Give the extent of all uninfected red blood cells.
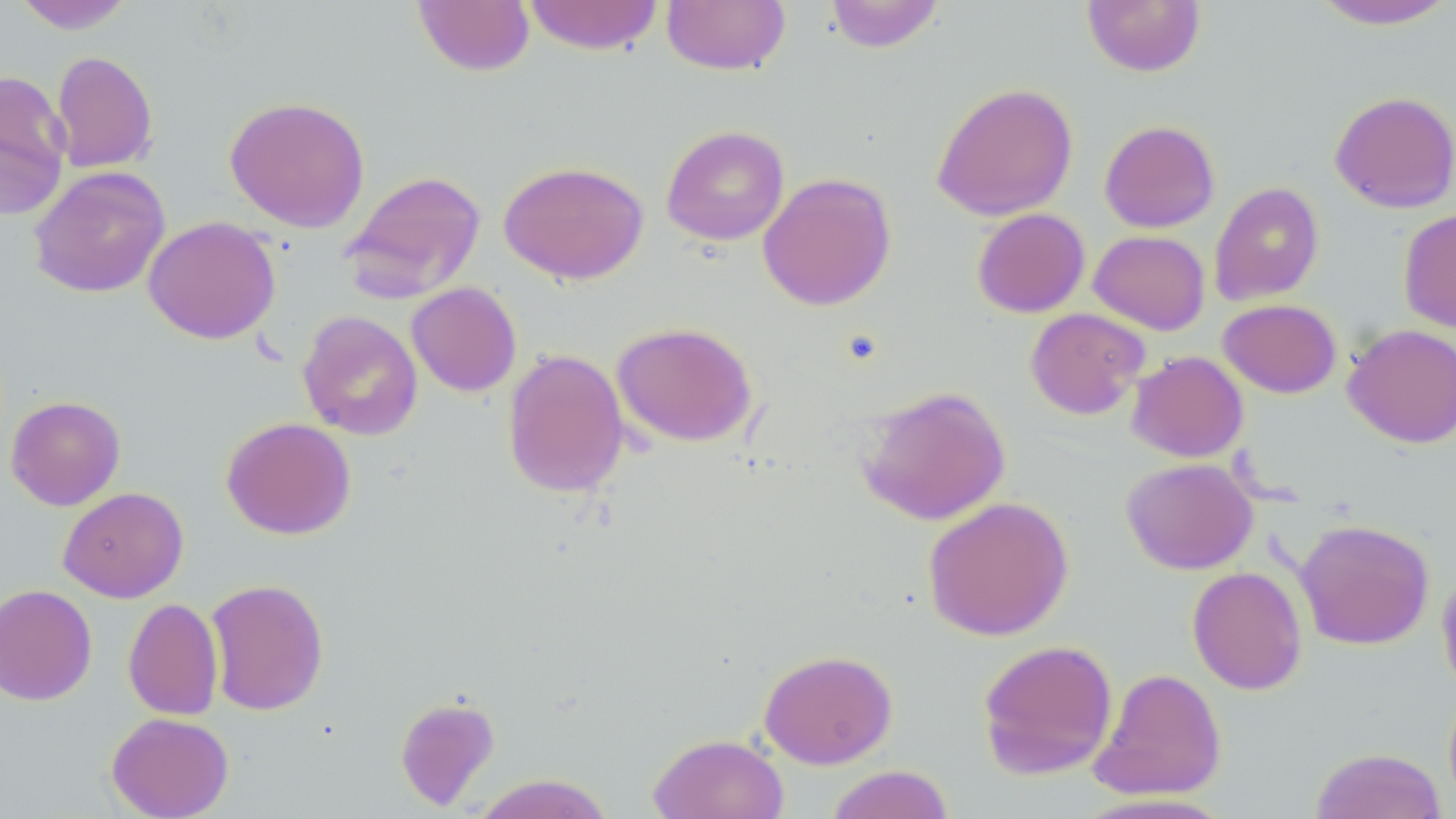
Approximate bounding boxes as (x1,y1)-(x2,y2) corner pairs in pixels.
Uninfected red blood cells: (521,0)-(665,55), (661,0)-(791,75), (823,0)-(946,53), (1082,0)-(1206,77), (1310,0)-(1456,31), (12,1)-(136,34), (412,1)-(535,76), (50,50)-(158,173), (0,70)-(72,222), (931,82)-(1079,221), (1329,90)-(1456,214), (224,95)-(370,232), (1099,120)-(1220,233), (660,124)-(790,245), (498,160)-(650,284), (29,166)-(170,299), (340,169)-(487,304), (758,172)-(896,311), (1209,182)-(1325,305), (972,207)-(1090,318), (1398,208)-(1456,333), (143,216)-(281,344), (1089,230)-(1210,335), (406,282)-(522,397), (1218,299)-(1342,398), (1025,307)-(1150,420), (297,310)-(423,441), (611,321)-(758,447), (1342,323)-(1456,449), (501,348)-(630,499), (1126,350)-(1249,462), (855,385)-(1011,526), (6,395)-(126,511), (221,416)-(356,540), (1121,457)-(1258,575), (58,486)-(188,603), (922,495)-(1074,641), (1294,518)-(1435,650), (1436,564)-(1456,698), (1187,565)-(1308,695), (205,578)-(329,716), (0,584)-(98,705), (123,597)-(223,720), (977,638)-(1118,781), (758,649)-(897,769), (1089,667)-(1228,801), (1443,685)-(1456,812), (395,695)-(500,811), (106,712)-(234,819), (648,733)-(789,819), (1310,747)-(1448,819), (826,765)-(955,819), (471,773)-(616,819).

Slide-level diagnosis: no evidence of blood parasites. Image is 1456×819 pixels. One field of a larger specimen. Thin blood film. Captured at 1000x magnification. Light microscopy. May-Grünwald-Giemsa stain.